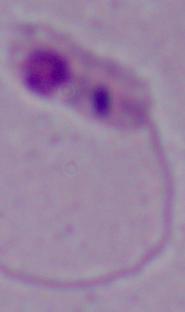

Photomicrograph. A Leishmania parasite is seen. Captured at 1000x magnification.